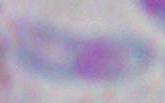
Toxoplasma gondii is seen. Photomicrograph. 1000x magnification.